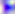
Summary:
  - Identification: Toxoplasma gondii
  - Modality: micrograph
  - Magnification: 400x